Name the blood parasite species.
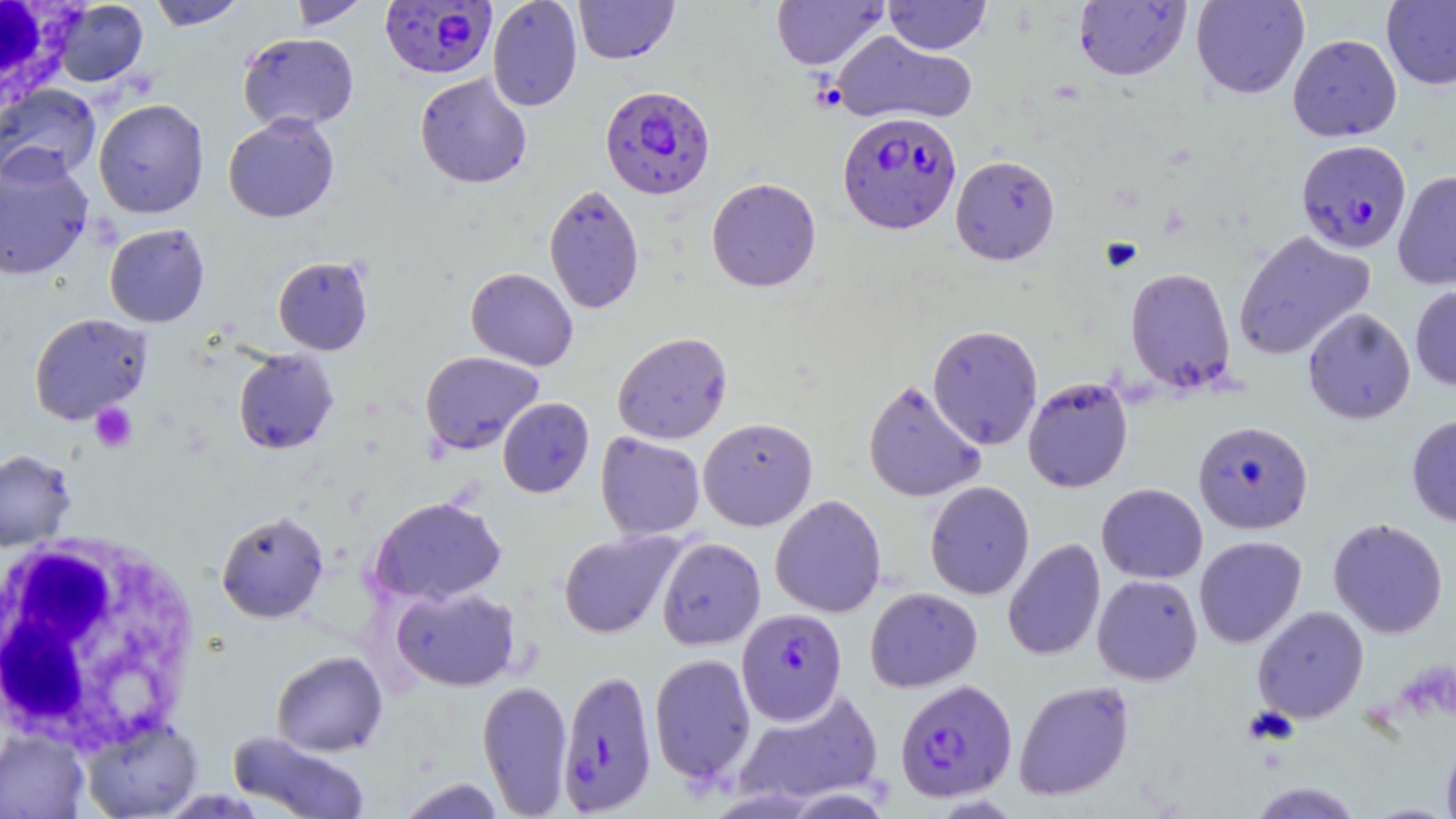
Plasmodium falciparum.

Approximate bounding boxes as (x1, y1, x2, y2) in pixels. Plasmodium falciparum-infected red blood cell locations: (381, 0, 497, 78), (600, 85, 715, 199), (838, 111, 962, 234), (1296, 139, 1412, 253), (1192, 420, 1313, 534), (736, 607, 847, 725), (562, 673, 663, 819), (894, 678, 1017, 803). White blood cell locations: (0, 1, 79, 113), (0, 531, 202, 753). Platelet locations: (90, 402, 137, 452). Uninfected red blood cell locations: (148, 0, 248, 30), (287, 0, 373, 30), (487, 0, 583, 112), (573, 0, 679, 64), (771, 0, 889, 70), (883, 0, 992, 54), (1191, 0, 1309, 99), (52, 1, 149, 87), (1073, 1, 1192, 81), (1381, 1, 1456, 90), (831, 30, 978, 127), (237, 32, 359, 132), (1287, 34, 1402, 142), (415, 73, 532, 189), (0, 84, 101, 187), (93, 97, 209, 218), (223, 113, 340, 223), (950, 154, 1060, 265), (0, 156, 94, 280), (1393, 170, 1456, 290), (706, 177, 821, 292), (543, 184, 645, 314), (104, 223, 210, 327), (1233, 229, 1376, 361), (273, 256, 373, 355), (1124, 266, 1236, 393), (465, 267, 578, 371), (1410, 283, 1456, 392), (1302, 307, 1416, 424), (29, 312, 153, 424), (927, 324, 1043, 450), (612, 331, 733, 444), (233, 349, 339, 454), (420, 351, 544, 454), (1022, 376, 1134, 493), (862, 378, 986, 503), (497, 397, 594, 497), (1406, 413, 1456, 527), (698, 417, 818, 531), (596, 432, 705, 540), (0, 449, 76, 552), (924, 481, 1035, 599), (1096, 482, 1208, 584), (770, 494, 887, 618), (369, 495, 507, 606), (215, 510, 329, 623), (1327, 517, 1449, 638), (558, 530, 683, 638), (1194, 535, 1307, 648), (656, 536, 766, 650), (1003, 537, 1106, 662), (1092, 574, 1203, 686), (390, 585, 521, 692), (864, 587, 982, 692), (1251, 604, 1370, 724), (271, 650, 388, 757), (649, 653, 756, 787), (477, 679, 573, 817), (1013, 679, 1135, 801), (733, 688, 885, 808), (80, 717, 204, 819), (0, 730, 89, 818), (229, 731, 370, 819), (1441, 733, 1456, 819), (397, 777, 507, 819), (1248, 781, 1363, 819). Thin blood film. Image is 1456×819 pixels. 1000x magnification. Optical microscopy. Single field of view. May-Grünwald-Giemsa-stained preparation.